Report the malaria status of this cell.
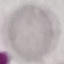

Uninfected.

Giemsa-stained preparation. Thin smear of blood. Acquired by smartphone through the microscope eyepiece. Automatically extracted cell patch, resized to 64 × 64 pixels.